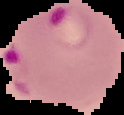

Summary:
  - Result: Plasmodium parasites detected
  - Image type: cell region segmented out of the field of view; surrounding area masked to black
  - Preparation: thin blood smear
  - Image size: 124×115 pixels